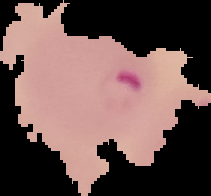

Malaria status: parasitized. Image is 211×196 pixels. From a thin blood smear. Segmented cell region on a black background.